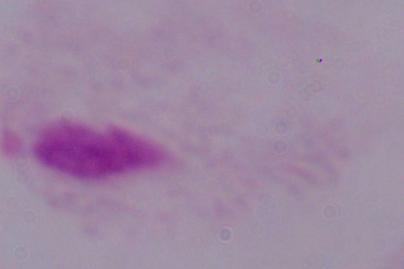
Summary:
  - Identification: trichomonad
  - Magnification: 1000x
  - Modality: photomicrograph